Report the malaria status of this cell.
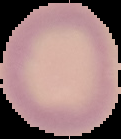
It is uninfected.

Summary:
  - Preparation: thin blood smear
  - Image size: 121×139 pixels
  - Image type: cell region segmented out of the field of view; surrounding area masked to black